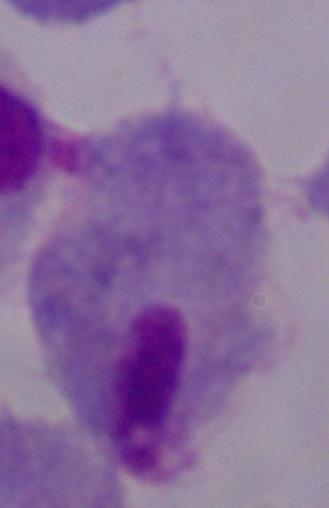
A trichomonad is shown. Photomicrograph. Captured at 1000x magnification.